Classify this cell by malaria status.
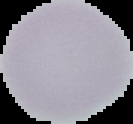

Uninfected.

Segmented cell region on a black background. Image is 133×124 pixels. From a thin blood smear.